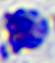

Summary:
  - Magnification: 400x
  - Identification: white blood cell
  - Modality: micrograph